Locate every Plasmodium ovale-infected red blood cell.
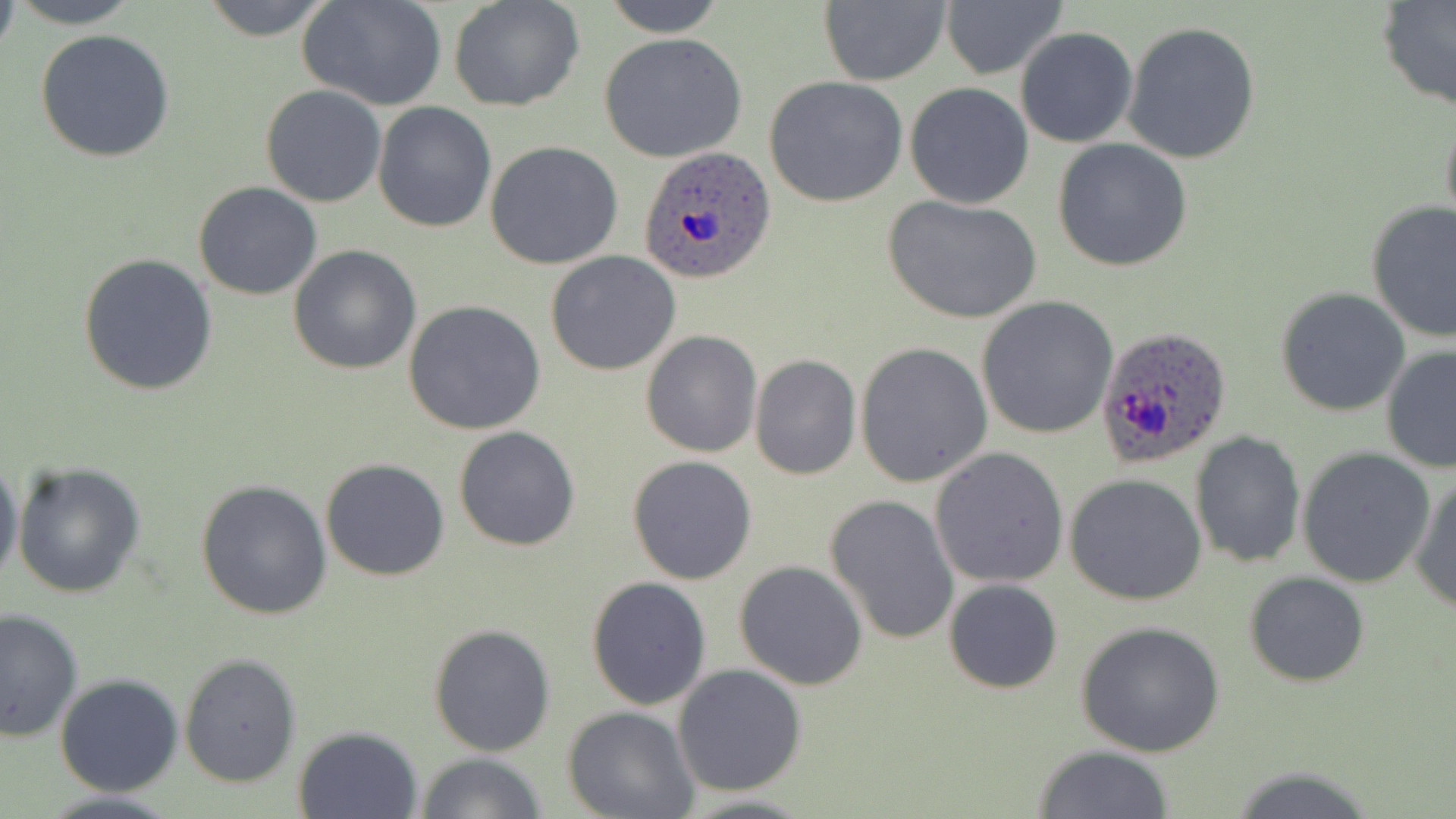

Approximate bounding boxes as (x1,y1)-(x2,y2) corner pairs in pixels.
Plasmodium ovale-infected red blood cells: (639,145)-(778,286), (1093,323)-(1234,469).

Uninfected red blood cell locations: (4,0)-(145,28), (198,0)-(338,41), (300,0)-(447,111), (448,0)-(585,114), (601,0)-(729,37), (818,1)-(950,86), (939,1)-(1062,81), (1377,1)-(1456,114), (1122,21)-(1260,164), (1016,28)-(1137,147), (35,29)-(176,164), (599,33)-(747,163), (764,75)-(910,209), (905,82)-(1034,209), (260,84)-(387,207), (372,101)-(496,232), (1439,112)-(1456,236), (1052,138)-(1193,270), (485,141)-(624,268), (192,182)-(322,301), (881,194)-(1041,324), (1365,201)-(1456,342), (288,245)-(421,375), (545,251)-(681,375), (78,254)-(220,397), (1276,288)-(1409,415), (975,295)-(1119,440), (404,300)-(549,436), (641,331)-(762,458), (854,341)-(992,487), (1381,347)-(1455,474), (750,354)-(861,480), (454,425)-(582,551), (1189,431)-(1305,568), (1296,446)-(1437,588), (930,448)-(1068,588), (0,455)-(22,593), (627,455)-(757,584), (320,458)-(450,581), (13,461)-(147,599), (1409,473)-(1456,613), (1064,474)-(1208,607), (195,478)-(333,620), (826,494)-(959,645), (734,560)-(868,689), (1243,571)-(1370,688), (586,575)-(712,710), (944,578)-(1064,694), (0,609)-(83,742), (1076,621)-(1226,758), (429,623)-(557,758), (179,653)-(302,788), (672,665)-(807,794), (54,674)-(185,795), (563,708)-(699,819), (292,726)-(423,818), (1032,745)-(1173,819), (415,753)-(547,819), (1222,766)-(1380,819), (34,789)-(186,819), (671,792)-(816,819). Slide-level diagnosis: Plasmodium ovale. May-Grünwald-Giemsa stain. Single field of view. Image is 1456×819 pixels. 1000x magnification. Optical microscopy. Thin blood smear.